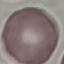

malaria status = uninfected
preparation = thin smear
capture = smartphone through the microscope eyepiece
image type = automatically extracted cell patch, resized to 64 × 64 pixels
stain = Giemsa